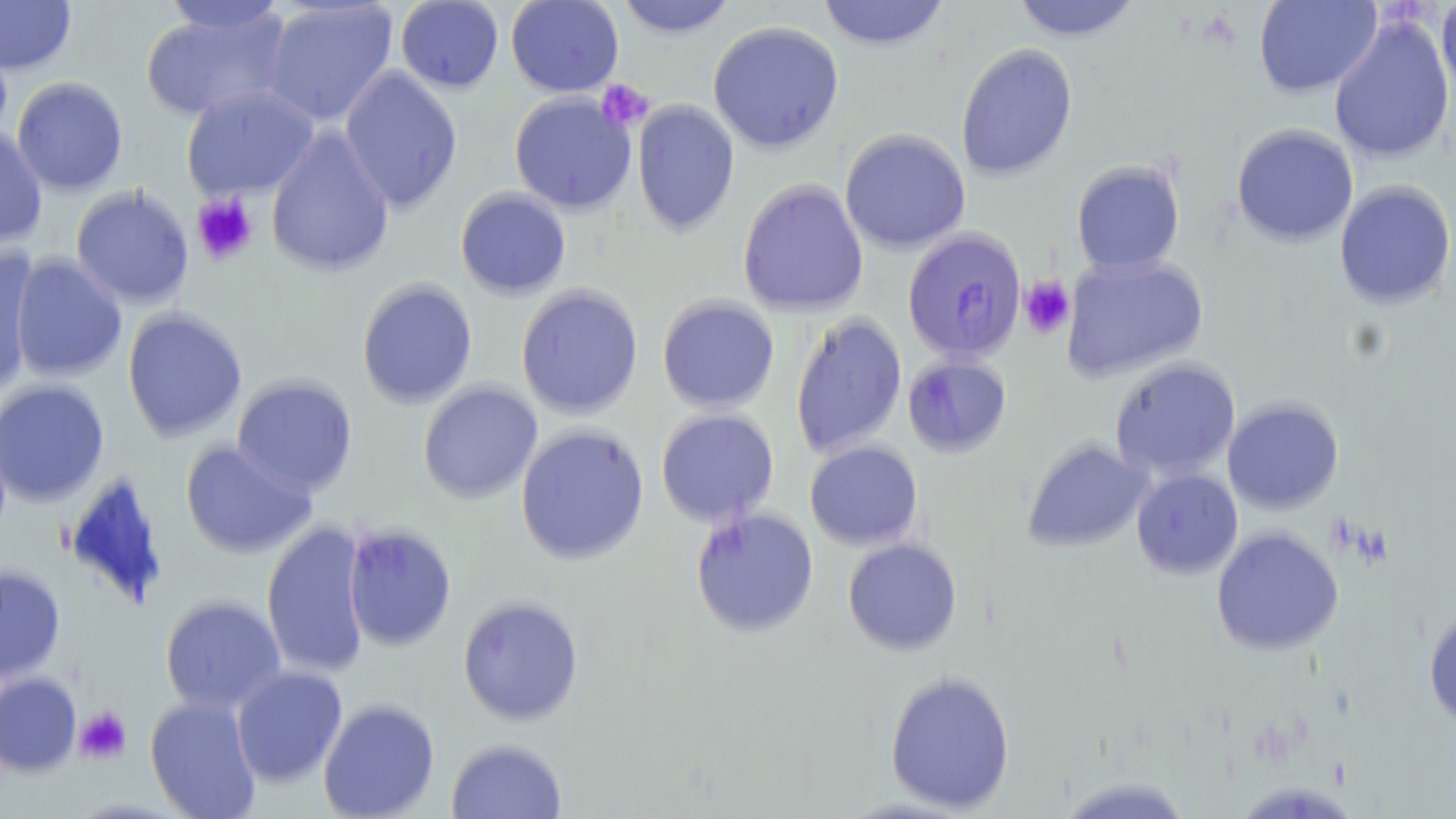

slide-level diagnosis = Plasmodium falciparum
stain = May-Grünwald-Giemsa
field of view = single
modality = optical microscopy
magnification = 1000x
preparation = thin blood smear
platelet locations = approximate bounding boxes as [x1, y1, x2, y2] in pixels: [596, 79, 653, 131], [191, 193, 258, 266], [1018, 277, 1075, 339], [73, 706, 131, 764]
uninfected red blood cell locations = approximate bounding boxes as [x1, y1, x2, y2] in pixels: [0, 0, 77, 75], [160, 0, 288, 36], [395, 0, 504, 93], [506, 0, 624, 97], [614, 0, 739, 38], [817, 0, 950, 51], [1010, 0, 1143, 41], [1253, 0, 1382, 98], [1436, 0, 1456, 104], [261, 1, 399, 127], [141, 6, 292, 122], [1328, 13, 1455, 164], [707, 20, 845, 153], [956, 43, 1078, 181], [338, 65, 463, 214], [12, 76, 128, 196], [181, 84, 320, 200], [509, 91, 637, 215], [631, 99, 740, 237], [0, 122, 48, 249], [1231, 123, 1359, 247], [265, 125, 395, 279], [839, 128, 971, 254], [1071, 159, 1186, 274], [737, 179, 869, 318], [1334, 180, 1456, 309], [70, 186, 195, 308], [455, 187, 572, 299], [0, 246, 39, 399], [10, 253, 127, 383], [1061, 253, 1209, 381], [356, 278, 478, 408], [515, 283, 644, 419], [657, 295, 780, 413], [122, 308, 248, 442], [790, 313, 908, 458], [902, 354, 1012, 457], [1109, 357, 1242, 482], [231, 374, 358, 496], [0, 379, 110, 506], [417, 382, 543, 504], [1222, 397, 1344, 514], [655, 408, 779, 527], [514, 424, 650, 566], [1022, 437, 1152, 553], [179, 439, 317, 559], [804, 440, 924, 551], [1131, 469, 1243, 579], [62, 472, 170, 609], [690, 507, 819, 638], [260, 520, 373, 680], [342, 523, 458, 652], [1211, 526, 1344, 656], [842, 538, 963, 656], [0, 564, 66, 684], [159, 595, 286, 714], [458, 595, 584, 725], [1423, 607, 1456, 731], [231, 665, 348, 787], [884, 671, 1016, 813], [0, 672, 82, 776], [145, 694, 262, 819], [318, 698, 440, 819], [446, 737, 567, 819], [1055, 776, 1194, 819]
Plasmodium falciparum-infected red blood cell locations = approximate bounding boxes as [x1, y1, x2, y2] in pixels: [902, 227, 1026, 363]
image size = 1456×819 pixels